Classify this cell by malaria status.
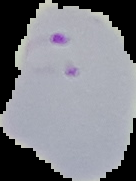
It is parasitized.

Image is 136×181 pixels. Cell region segmented out of the field of view; the surrounding area is masked to black. From a thin blood smear.